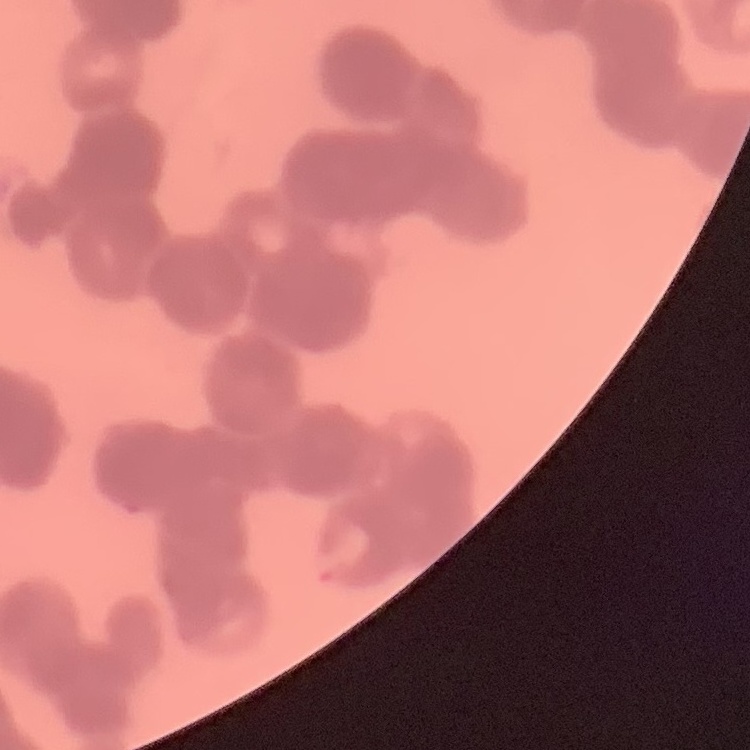
The red blood cells exhibit rouleaux formation. Field's or Giemsa stain. One tile cut from a larger photomicrograph. Thin blood smear.